Classify this cell by malaria status.
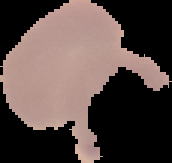

It is uninfected.

Summary:
  - Image type: segmented cell region on a black background
  - Image size: 172×163 pixels
  - Preparation: thin blood smear